Locate every blood parasite and identify its species.
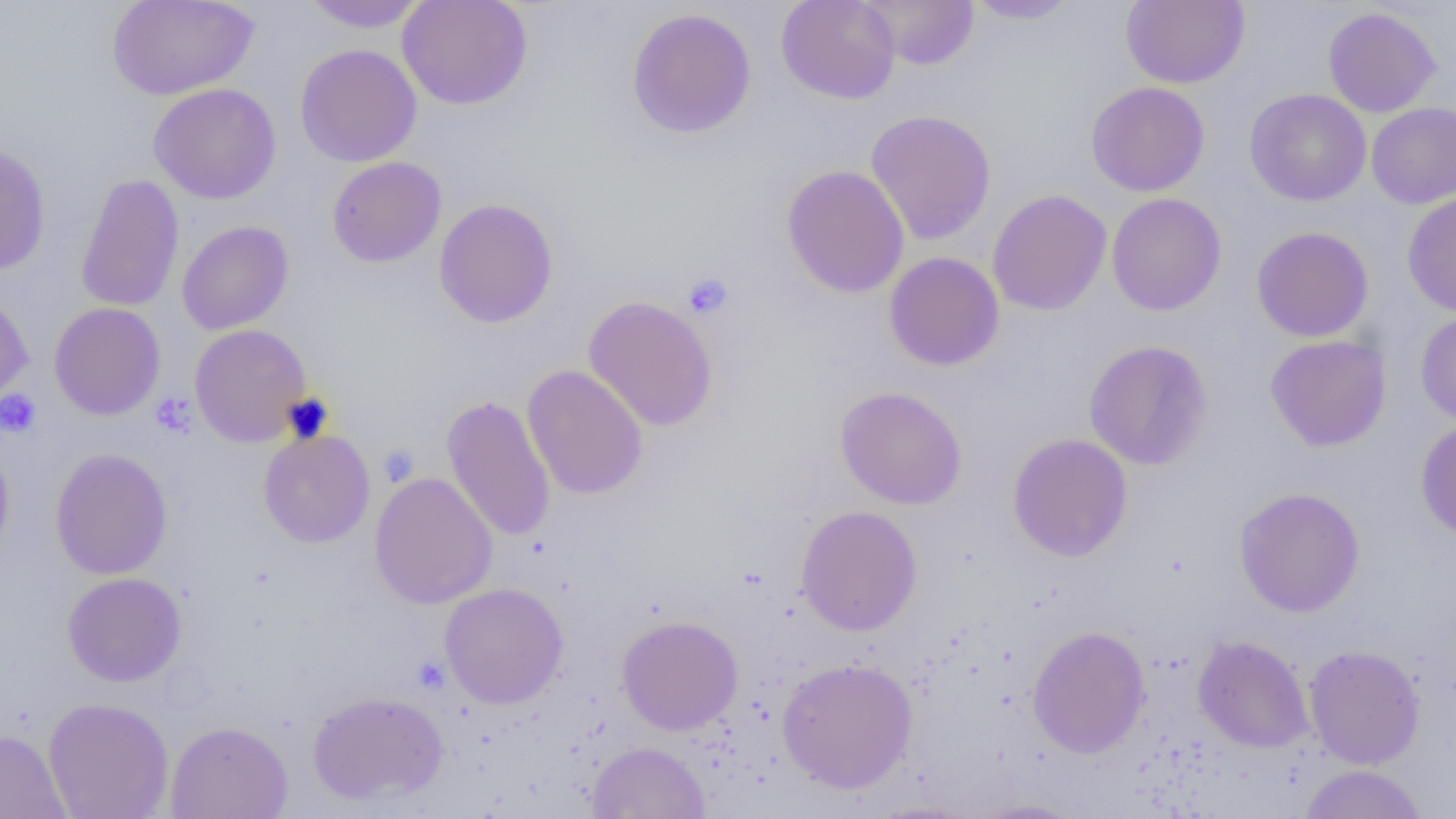
No blood parasites observed.

slide-level diagnosis = negative for blood parasites
preparation = thin blood smear
field of view = one of a larger specimen
modality = light microscopy
platelet locations = approximate bounding boxes as (x1,y1)-(x2,y2) corner pairs in pixels: (683,273)-(734,319), (0,389)-(41,437), (150,393)-(197,437), (378,444)-(419,487), (413,656)-(450,694)
image size = 1456×819 pixels
magnification = 1000x
uninfected red blood cell locations = approximate bounding boxes as (x1,y1)-(x2,y2) corner pairs in pixels: (106,0)-(259,100), (397,0)-(533,110), (776,0)-(901,104), (860,0)-(979,70), (965,0)-(1080,24), (1120,0)-(1250,88), (300,1)-(427,32), (1323,6)-(1441,118), (626,8)-(757,139), (295,44)-(422,167), (1085,81)-(1210,197), (148,83)-(282,204), (1244,88)-(1372,206), (1366,102)-(1456,209), (865,109)-(997,245), (0,142)-(51,276), (327,156)-(446,267), (782,165)-(909,298), (76,173)-(184,313), (987,189)-(1112,316), (1401,191)-(1456,318), (1107,193)-(1227,316), (433,198)-(559,328), (176,220)-(294,335), (1251,226)-(1374,342), (884,251)-(1005,371), (0,287)-(33,409), (583,296)-(718,431), (49,302)-(166,420), (1415,310)-(1456,426), (189,323)-(312,447), (1265,334)-(1392,452), (1083,340)-(1213,470), (522,365)-(648,500), (835,386)-(967,509), (441,395)-(556,542), (1415,417)-(1456,541), (259,428)-(375,548), (1007,433)-(1133,562), (0,443)-(14,567), (49,448)-(173,580), (370,472)-(497,609), (1233,487)-(1365,617), (795,505)-(923,636), (62,572)-(187,687), (440,582)-(569,709), (616,615)-(744,735), (1027,625)-(1150,758), (1193,635)-(1314,752), (1303,644)-(1426,769), (776,657)-(919,794), (308,690)-(448,806), (43,697)-(174,818), (165,720)-(293,819), (0,728)-(70,819), (587,741)-(710,819), (1298,764)-(1428,818), (968,798)-(1090,818)